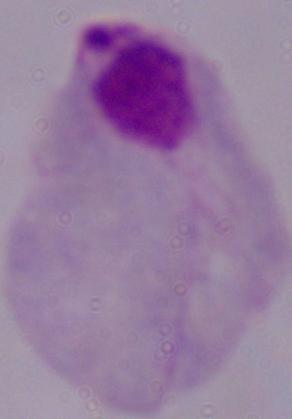

{
  "modality": "micrograph",
  "magnification": "1000x",
  "identification": "trichomonad"
}